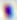
{
  "modality": "micrograph",
  "magnification": "400x",
  "identification": "Toxoplasma gondii"
}